State the blood parasite species.
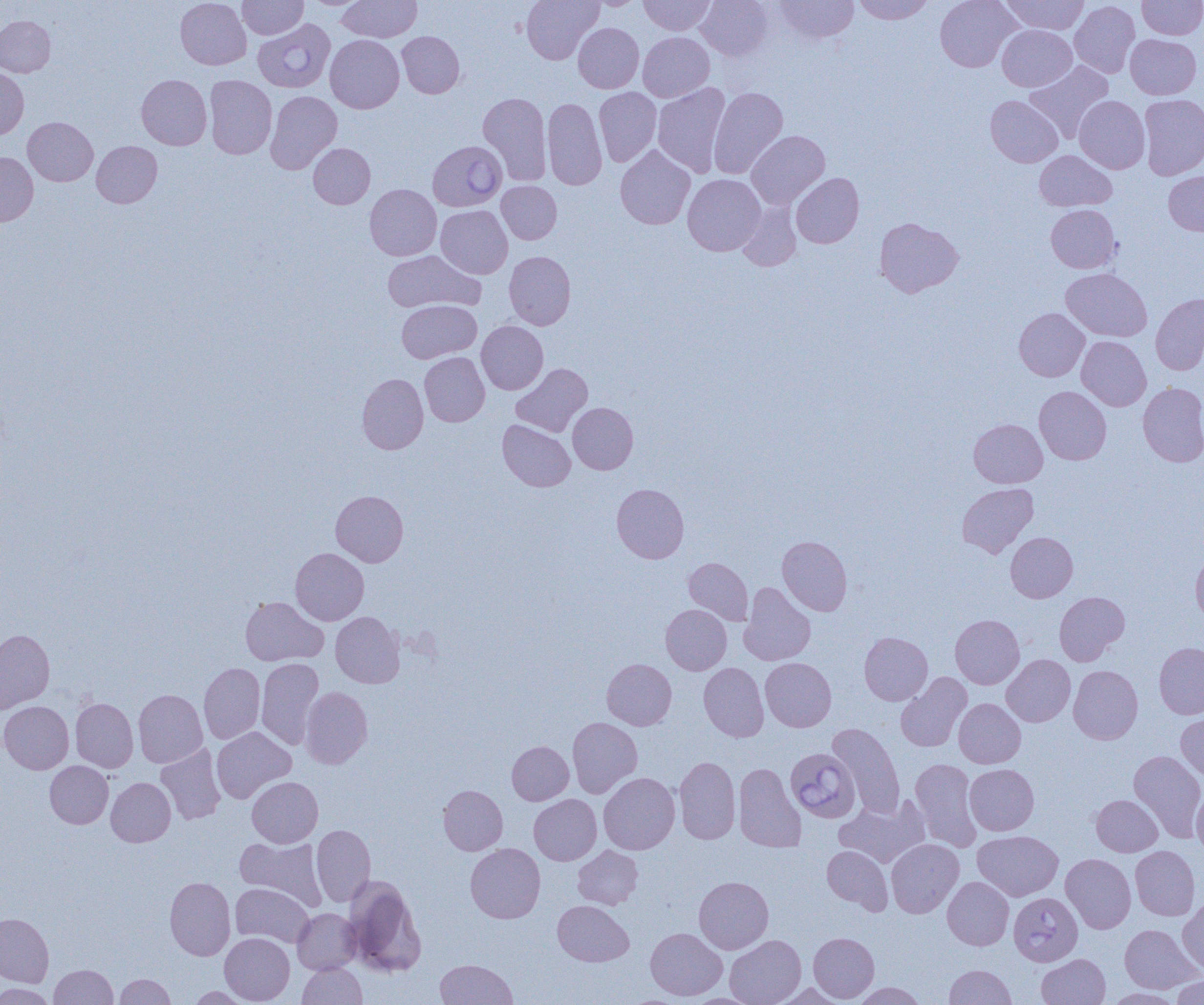

Babesia divergens.

Summary:
  - Coordinate format: approximate bounding boxes as named x1/y1/x2/y2 corners in pixels
  - Babesia divergens-infected red blood cell locations: (x1=253, y1=19, x2=335, y2=92), (x1=428, y1=140, x2=507, y2=211), (x1=786, y1=748, x2=860, y2=823), (x1=1009, y1=892, x2=1082, y2=965)
  - Uninfected red blood cell locations: (x1=175, y1=0, x2=251, y2=69), (x1=238, y1=0, x2=308, y2=39), (x1=303, y1=0, x2=370, y2=9), (x1=337, y1=0, x2=422, y2=42), (x1=522, y1=0, x2=604, y2=64), (x1=582, y1=0, x2=647, y2=10), (x1=639, y1=0, x2=715, y2=35), (x1=696, y1=0, x2=773, y2=61), (x1=774, y1=0, x2=858, y2=44), (x1=853, y1=0, x2=934, y2=24), (x1=935, y1=0, x2=1020, y2=72), (x1=1001, y1=0, x2=1089, y2=34), (x1=1137, y1=0, x2=1204, y2=39), (x1=1070, y1=1, x2=1140, y2=78), (x1=0, y1=15, x2=55, y2=77), (x1=573, y1=23, x2=644, y2=93), (x1=997, y1=25, x2=1076, y2=91), (x1=397, y1=31, x2=464, y2=98), (x1=638, y1=31, x2=714, y2=102), (x1=1126, y1=34, x2=1201, y2=99), (x1=326, y1=35, x2=404, y2=113), (x1=1024, y1=60, x2=1114, y2=143), (x1=0, y1=67, x2=29, y2=139), (x1=136, y1=74, x2=212, y2=150), (x1=205, y1=75, x2=277, y2=159), (x1=652, y1=83, x2=730, y2=177), (x1=594, y1=87, x2=661, y2=166), (x1=708, y1=87, x2=788, y2=179), (x1=266, y1=90, x2=342, y2=173), (x1=478, y1=92, x2=552, y2=185), (x1=1139, y1=94, x2=1204, y2=180), (x1=986, y1=95, x2=1062, y2=167), (x1=1074, y1=95, x2=1150, y2=173), (x1=542, y1=98, x2=607, y2=190), (x1=22, y1=117, x2=98, y2=186), (x1=746, y1=130, x2=830, y2=209), (x1=92, y1=141, x2=162, y2=207), (x1=309, y1=143, x2=375, y2=208), (x1=615, y1=145, x2=696, y2=229), (x1=1035, y1=150, x2=1117, y2=212), (x1=0, y1=152, x2=38, y2=227), (x1=1164, y1=171, x2=1204, y2=236), (x1=791, y1=173, x2=864, y2=248), (x1=682, y1=174, x2=766, y2=256), (x1=497, y1=181, x2=562, y2=244), (x1=365, y1=184, x2=441, y2=260), (x1=737, y1=201, x2=802, y2=271), (x1=1046, y1=204, x2=1120, y2=273), (x1=436, y1=205, x2=513, y2=278), (x1=875, y1=217, x2=963, y2=297), (x1=383, y1=250, x2=483, y2=313), (x1=504, y1=251, x2=576, y2=330), (x1=1061, y1=268, x2=1152, y2=342), (x1=1150, y1=293, x2=1204, y2=375), (x1=397, y1=300, x2=481, y2=363), (x1=1014, y1=308, x2=1089, y2=381), (x1=477, y1=321, x2=548, y2=394), (x1=1077, y1=336, x2=1151, y2=411), (x1=420, y1=352, x2=490, y2=426), (x1=511, y1=363, x2=592, y2=436), (x1=357, y1=373, x2=428, y2=454), (x1=1138, y1=382, x2=1204, y2=466), (x1=1034, y1=386, x2=1111, y2=464), (x1=568, y1=402, x2=638, y2=474), (x1=497, y1=419, x2=575, y2=491), (x1=969, y1=419, x2=1047, y2=488), (x1=957, y1=482, x2=1038, y2=557), (x1=612, y1=483, x2=689, y2=563), (x1=331, y1=490, x2=408, y2=566), (x1=1006, y1=532, x2=1077, y2=602), (x1=777, y1=536, x2=852, y2=616), (x1=291, y1=547, x2=369, y2=625), (x1=1191, y1=551, x2=1204, y2=624), (x1=683, y1=557, x2=754, y2=625), (x1=739, y1=582, x2=815, y2=665), (x1=1054, y1=591, x2=1129, y2=665), (x1=240, y1=596, x2=327, y2=665), (x1=661, y1=604, x2=731, y2=675), (x1=330, y1=612, x2=405, y2=688), (x1=950, y1=614, x2=1024, y2=689), (x1=0, y1=629, x2=54, y2=713), (x1=859, y1=632, x2=932, y2=705), (x1=1154, y1=642, x2=1204, y2=719), (x1=1002, y1=654, x2=1075, y2=727), (x1=256, y1=658, x2=324, y2=748), (x1=602, y1=658, x2=676, y2=730), (x1=761, y1=658, x2=836, y2=731), (x1=199, y1=663, x2=265, y2=743), (x1=699, y1=663, x2=768, y2=741), (x1=1068, y1=665, x2=1143, y2=743), (x1=895, y1=673, x2=971, y2=752), (x1=301, y1=686, x2=372, y2=768), (x1=133, y1=689, x2=207, y2=767), (x1=70, y1=698, x2=138, y2=772), (x1=954, y1=698, x2=1025, y2=768), (x1=0, y1=701, x2=74, y2=773), (x1=1176, y1=712, x2=1204, y2=780), (x1=567, y1=717, x2=642, y2=798), (x1=828, y1=723, x2=905, y2=818), (x1=211, y1=726, x2=296, y2=803), (x1=507, y1=741, x2=573, y2=804), (x1=156, y1=744, x2=227, y2=824), (x1=1129, y1=750, x2=1204, y2=841), (x1=674, y1=757, x2=741, y2=844), (x1=910, y1=758, x2=982, y2=851), (x1=45, y1=761, x2=113, y2=828), (x1=733, y1=762, x2=805, y2=852), (x1=964, y1=764, x2=1039, y2=835), (x1=599, y1=772, x2=680, y2=854), (x1=106, y1=777, x2=175, y2=846), (x1=247, y1=777, x2=323, y2=847), (x1=438, y1=785, x2=507, y2=855), (x1=1192, y1=788, x2=1204, y2=856), (x1=529, y1=794, x2=601, y2=865), (x1=1091, y1=794, x2=1163, y2=856), (x1=835, y1=796, x2=931, y2=868), (x1=311, y1=825, x2=375, y2=906), (x1=973, y1=830, x2=1063, y2=900), (x1=236, y1=836, x2=326, y2=910), (x1=886, y1=839, x2=963, y2=918), (x1=465, y1=843, x2=545, y2=923), (x1=573, y1=845, x2=643, y2=909), (x1=822, y1=845, x2=892, y2=914), (x1=1130, y1=845, x2=1200, y2=920), (x1=1061, y1=854, x2=1136, y2=933), (x1=165, y1=876, x2=236, y2=960), (x1=694, y1=876, x2=774, y2=953), (x1=943, y1=877, x2=1013, y2=950), (x1=344, y1=878, x2=426, y2=976), (x1=230, y1=883, x2=314, y2=947), (x1=1178, y1=897, x2=1204, y2=975), (x1=553, y1=900, x2=633, y2=966), (x1=292, y1=908, x2=361, y2=974), (x1=0, y1=913, x2=53, y2=987), (x1=1119, y1=924, x2=1201, y2=993), (x1=645, y1=927, x2=727, y2=1000), (x1=809, y1=932, x2=879, y2=1002), (x1=220, y1=933, x2=294, y2=1004), (x1=725, y1=935, x2=806, y2=1005), (x1=1037, y1=954, x2=1110, y2=1005), (x1=435, y1=959, x2=518, y2=1004), (x1=298, y1=962, x2=366, y2=1005), (x1=50, y1=964, x2=117, y2=1004), (x1=944, y1=965, x2=1016, y2=1004), (x1=115, y1=974, x2=175, y2=1005), (x1=1170, y1=975, x2=1204, y2=1004), (x1=772, y1=982, x2=847, y2=1004), (x1=852, y1=982, x2=927, y2=1004), (x1=0, y1=983, x2=55, y2=1005), (x1=186, y1=986, x2=253, y2=1004), (x1=1102, y1=988, x2=1185, y2=1004)
  - Modality: light microscopy
  - Preparation: thin blood smear
  - Magnification: 1000x
  - Image size: 1204×1005 pixels
  - Field of view: single